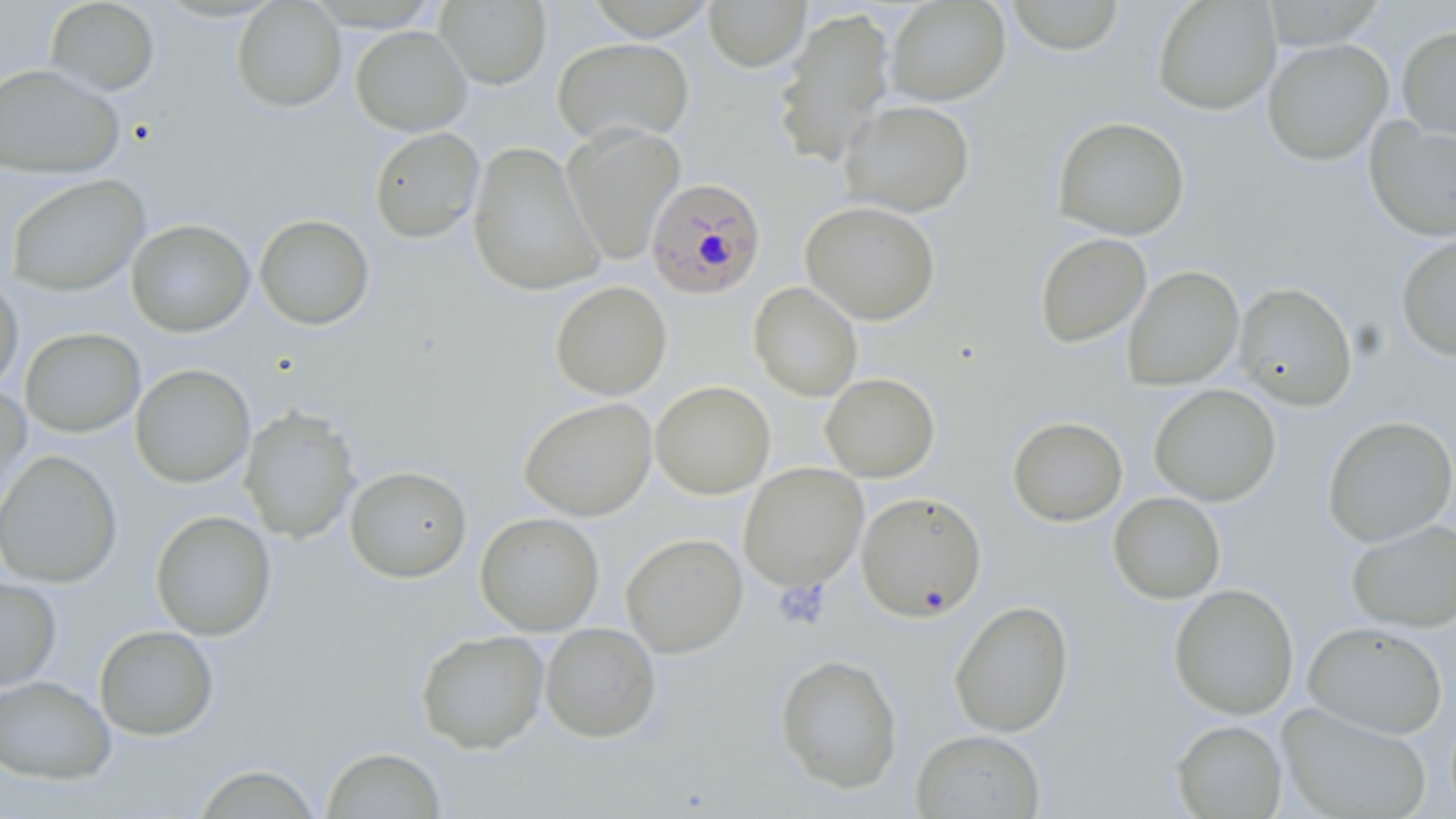

slide-level diagnosis = Plasmodium falciparum
stain = May-Grünwald-Giemsa
uninfected red blood cell locations = approximate bounding boxes as named x1/y1/x2/y2 corners in pixels: (x1=44, y1=0, x2=160, y2=96), (x1=232, y1=0, x2=347, y2=113), (x1=584, y1=0, x2=717, y2=41), (x1=704, y1=0, x2=811, y2=72), (x1=885, y1=0, x2=1010, y2=106), (x1=1005, y1=0, x2=1126, y2=55), (x1=1152, y1=0, x2=1281, y2=115), (x1=435, y1=1, x2=551, y2=90), (x1=772, y1=6, x2=897, y2=168), (x1=1396, y1=25, x2=1456, y2=140), (x1=351, y1=26, x2=472, y2=136), (x1=553, y1=37, x2=694, y2=146), (x1=1262, y1=38, x2=1394, y2=166), (x1=0, y1=63, x2=125, y2=178), (x1=839, y1=99, x2=975, y2=218), (x1=1052, y1=116, x2=1190, y2=240), (x1=1365, y1=119, x2=1456, y2=241), (x1=562, y1=122, x2=685, y2=265), (x1=369, y1=126, x2=485, y2=244), (x1=467, y1=142, x2=605, y2=297), (x1=5, y1=174, x2=151, y2=297), (x1=800, y1=200, x2=941, y2=325), (x1=254, y1=213, x2=375, y2=330), (x1=126, y1=218, x2=255, y2=337), (x1=1034, y1=232, x2=1152, y2=349), (x1=1396, y1=233, x2=1456, y2=361), (x1=1122, y1=265, x2=1244, y2=391), (x1=0, y1=277, x2=23, y2=393), (x1=550, y1=281, x2=672, y2=400), (x1=748, y1=282, x2=863, y2=402), (x1=1232, y1=282, x2=1357, y2=411), (x1=20, y1=327, x2=146, y2=438), (x1=130, y1=363, x2=256, y2=488), (x1=820, y1=373, x2=940, y2=482), (x1=650, y1=380, x2=775, y2=499), (x1=0, y1=383, x2=31, y2=520), (x1=1148, y1=383, x2=1282, y2=506), (x1=519, y1=397, x2=657, y2=521), (x1=240, y1=405, x2=362, y2=543), (x1=1322, y1=415, x2=1456, y2=547), (x1=1007, y1=416, x2=1128, y2=527), (x1=0, y1=449, x2=123, y2=589), (x1=739, y1=463, x2=868, y2=591), (x1=345, y1=465, x2=472, y2=583), (x1=856, y1=491, x2=987, y2=622), (x1=1108, y1=491, x2=1226, y2=604), (x1=150, y1=510, x2=276, y2=641), (x1=475, y1=512, x2=604, y2=636), (x1=1346, y1=519, x2=1456, y2=633), (x1=621, y1=533, x2=748, y2=658), (x1=0, y1=576, x2=62, y2=692), (x1=1168, y1=583, x2=1299, y2=719), (x1=949, y1=600, x2=1074, y2=738), (x1=1303, y1=621, x2=1449, y2=739), (x1=540, y1=622, x2=662, y2=743), (x1=94, y1=625, x2=219, y2=741), (x1=415, y1=629, x2=549, y2=754), (x1=774, y1=653, x2=903, y2=794), (x1=0, y1=675, x2=116, y2=785), (x1=1276, y1=702, x2=1433, y2=819), (x1=1170, y1=719, x2=1287, y2=818), (x1=911, y1=728, x2=1046, y2=818), (x1=321, y1=746, x2=447, y2=818), (x1=191, y1=763, x2=324, y2=818)
Plasmodium falciparum-infected red blood cell locations = approximate bounding boxes as named x1/y1/x2/y2 corners in pixels: (x1=642, y1=176, x2=767, y2=299)
image size = 1456×819 pixels
field of view = one of a larger specimen
modality = optical microscopy
preparation = thin blood film
platelet locations = approximate bounding boxes as named x1/y1/x2/y2 corners in pixels: (x1=773, y1=579, x2=831, y2=631)
magnification = 1000x